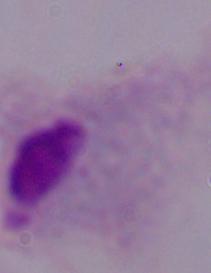

Summary:
  - Magnification: 1000x
  - Identification: trichomonad
  - Modality: micrograph